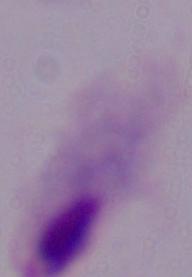
A trichomonad is shown. Micrograph. Captured at 1000x magnification.